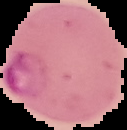
result = Plasmodium parasites identified
image size = 127×130 pixels
preparation = thin blood smear
image type = segmented cell region with the area outside set to black